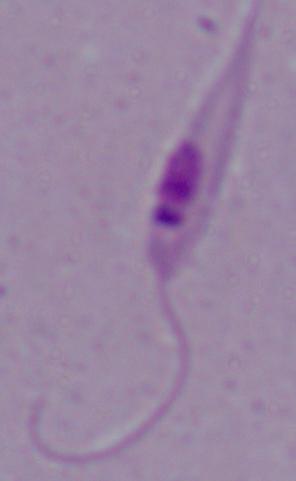 A Leishmania parasite is shown. Micrograph. Captured at 1000x magnification.